Name the parasite shown.
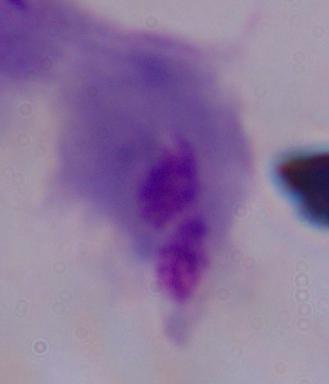

A trichomonad.

modality: micrograph
magnification: 1000x